Point out each Plasmodium parasite and each leukocyte.
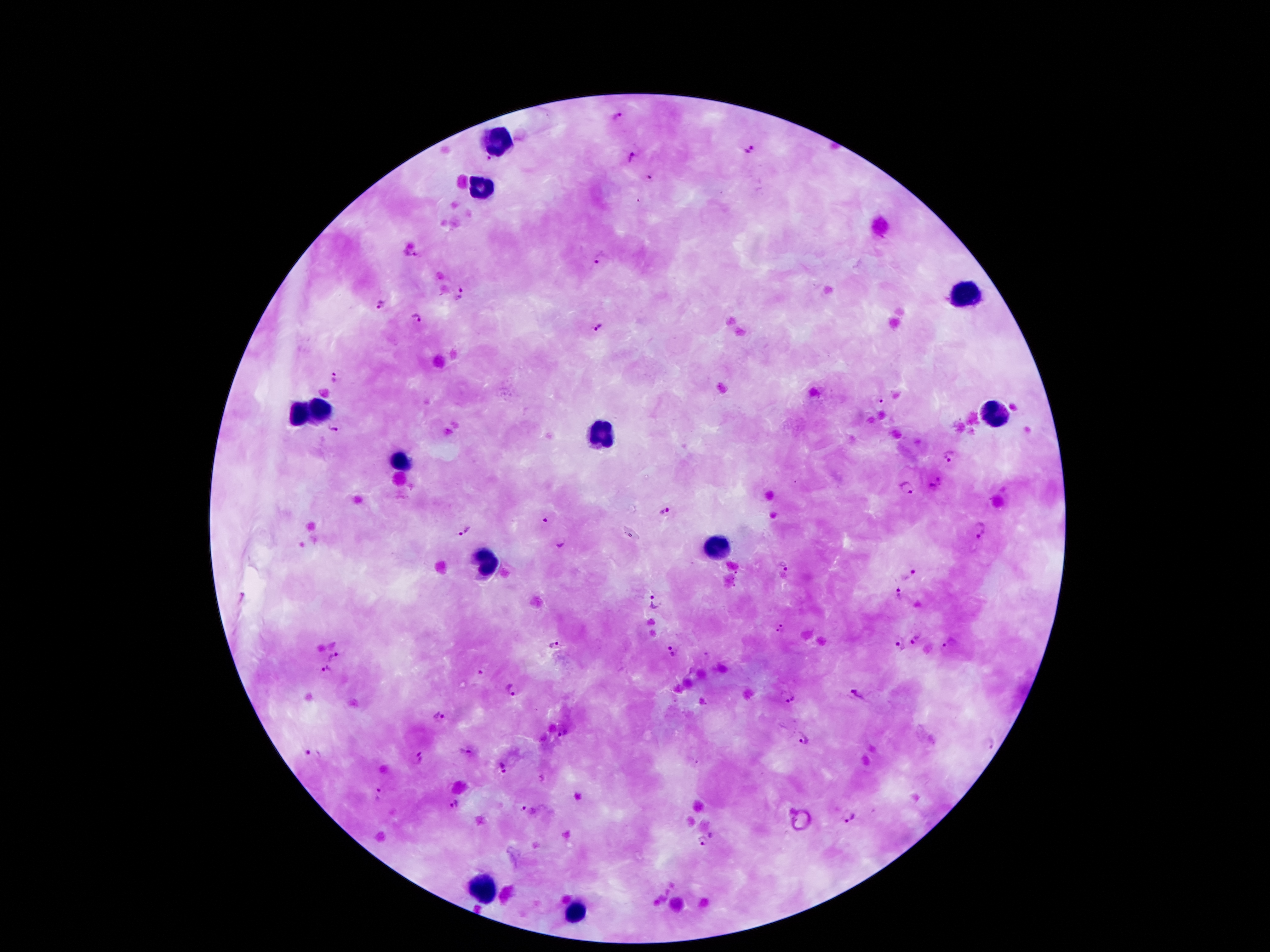

Approximate object centers, in pixels from the top-left corner.
Plasmodium parasites: (x=620, y=117), (x=748, y=152), (x=630, y=159), (x=650, y=179), (x=416, y=254), (x=600, y=257), (x=462, y=294), (x=383, y=305), (x=418, y=318), (x=595, y=327), (x=333, y=377), (x=878, y=398), (x=332, y=429), (x=951, y=456), (x=936, y=484), (x=905, y=487), (x=664, y=514), (x=546, y=519), (x=465, y=529), (x=980, y=531), (x=561, y=544), (x=781, y=566), (x=907, y=573), (x=899, y=594), (x=654, y=601), (x=781, y=628), (x=915, y=640), (x=895, y=642), (x=554, y=644), (x=947, y=644), (x=673, y=650), (x=332, y=654), (x=324, y=669), (x=479, y=674), (x=511, y=690), (x=856, y=695), (x=786, y=698), (x=438, y=717), (x=803, y=736), (x=986, y=746), (x=467, y=751), (x=311, y=753), (x=420, y=761), (x=504, y=769), (x=377, y=796), (x=456, y=803), (x=521, y=808), (x=850, y=817), (x=712, y=835), (x=699, y=843).
Leukocytes: (x=498, y=141), (x=479, y=187), (x=970, y=296), (x=993, y=412), (x=317, y=414), (x=298, y=416), (x=599, y=431), (x=401, y=460), (x=714, y=546), (x=485, y=565), (x=481, y=891), (x=576, y=916).

Summary:
  - Preparation: thick peripheral-blood smear
  - Capture: smartphone through the microscope eyepiece
  - Patient malaria status: infected with Plasmodium falciparum
  - Field of view: single
  - Image size: 1270×952 pixels
  - Stain: Giemsa
  - Magnification: 100x